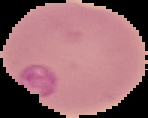
Summary:
  - Image type: cell region segmented out of the field of view; surrounding area masked to black
  - Malaria status: parasitized
  - Preparation: thin blood smear
  - Image size: 148×118 pixels